Comment on the morphology of the erythrocytes.
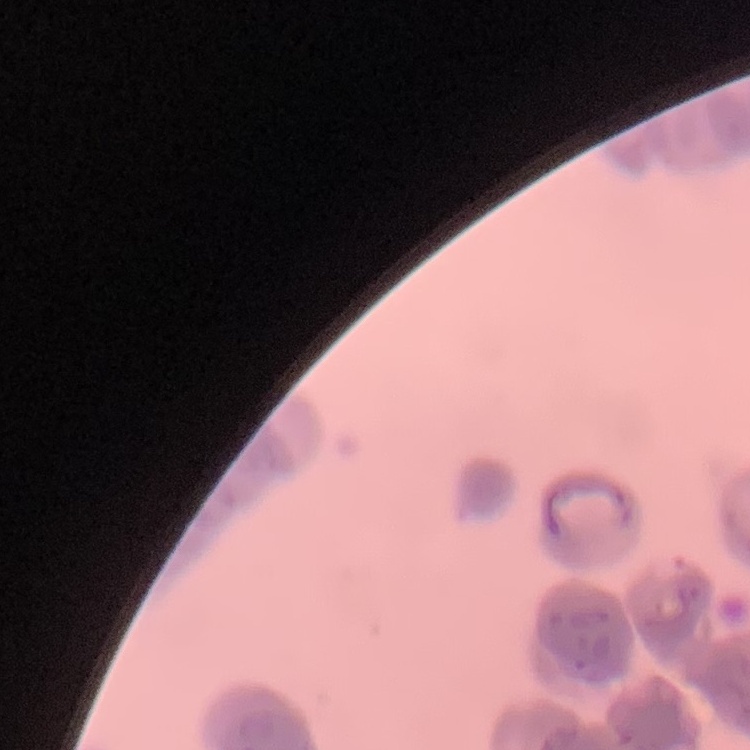

Rouleaux formation.

stain = Field's or Giemsa
image type = square crop of a larger photomicrograph
preparation = thin peripheral smear